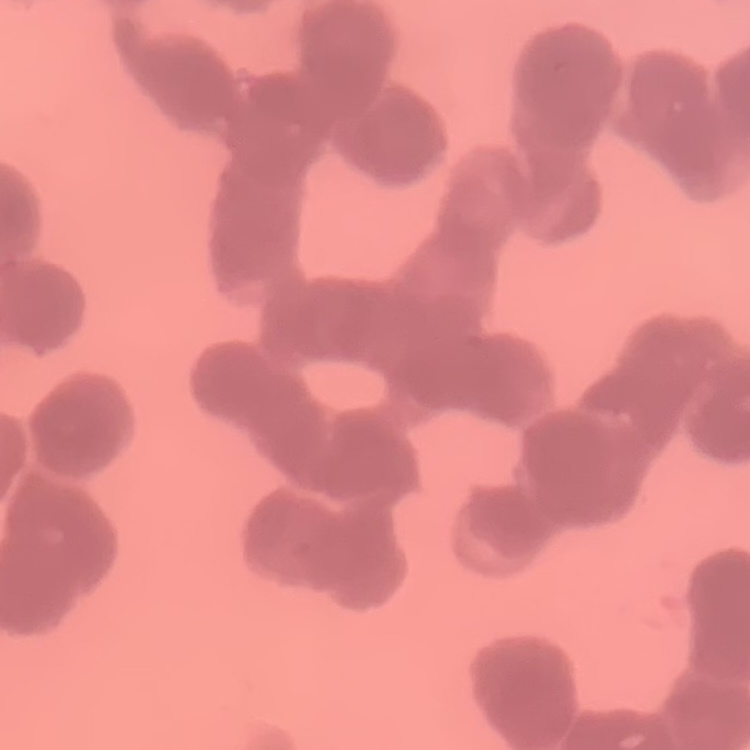

red blood cell morphology = rouleaux formation
preparation = thin blood smear
stain = Field's or Giemsa
image type = square crop of a larger photomicrograph